Describe the morphology of the red blood cells.
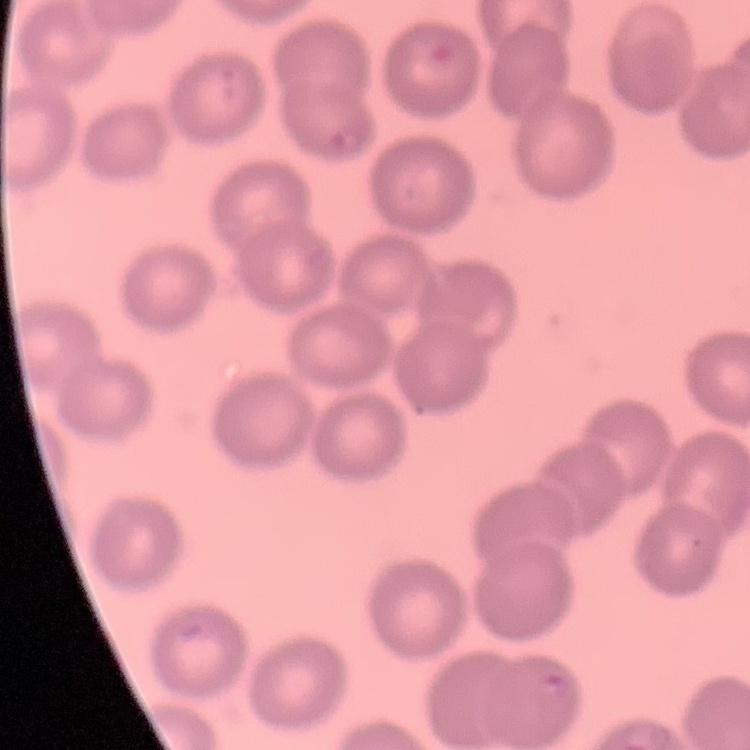
They show no rouleaux formation.

Square crop of a larger photomicrograph. Stained with either Field's or Giemsa. Thin blood film.